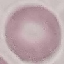 Result: no malaria parasites detected. Cell patch, automatically extracted from a larger field of view and resized to 64 × 64 pixels. Giemsa-stained preparation. Acquired by smartphone through the microscope eyepiece. Thin blood smear.